Assess the morphology of the erythrocytes.
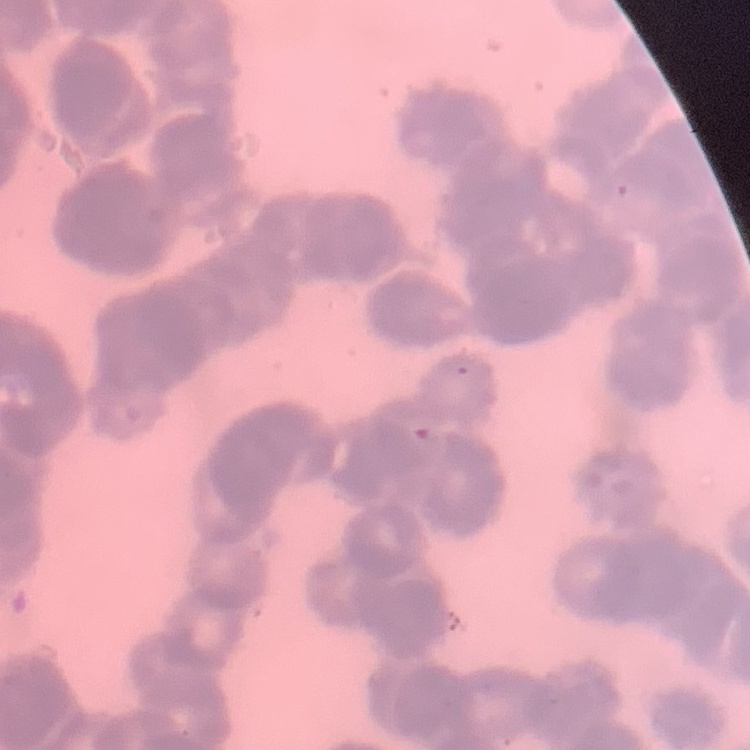

Rouleaux formation.

Field's or Giemsa stain. Thin peripheral smear. One tile cut from a larger photomicrograph.